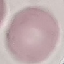

result = no malaria parasites detected
preparation = thin blood smear
image type = cell patch, automatically extracted from a larger field of view and resized to 64 × 64 pixels
capture = smartphone camera at the microscope eyepiece
stain = Giemsa